Report the malaria status of this cell.
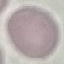
Uninfected.

Automatically extracted cell patch, resized to 64 × 64 pixels. Thin blood smear. Giemsa stain. Acquired by smartphone through the microscope eyepiece.